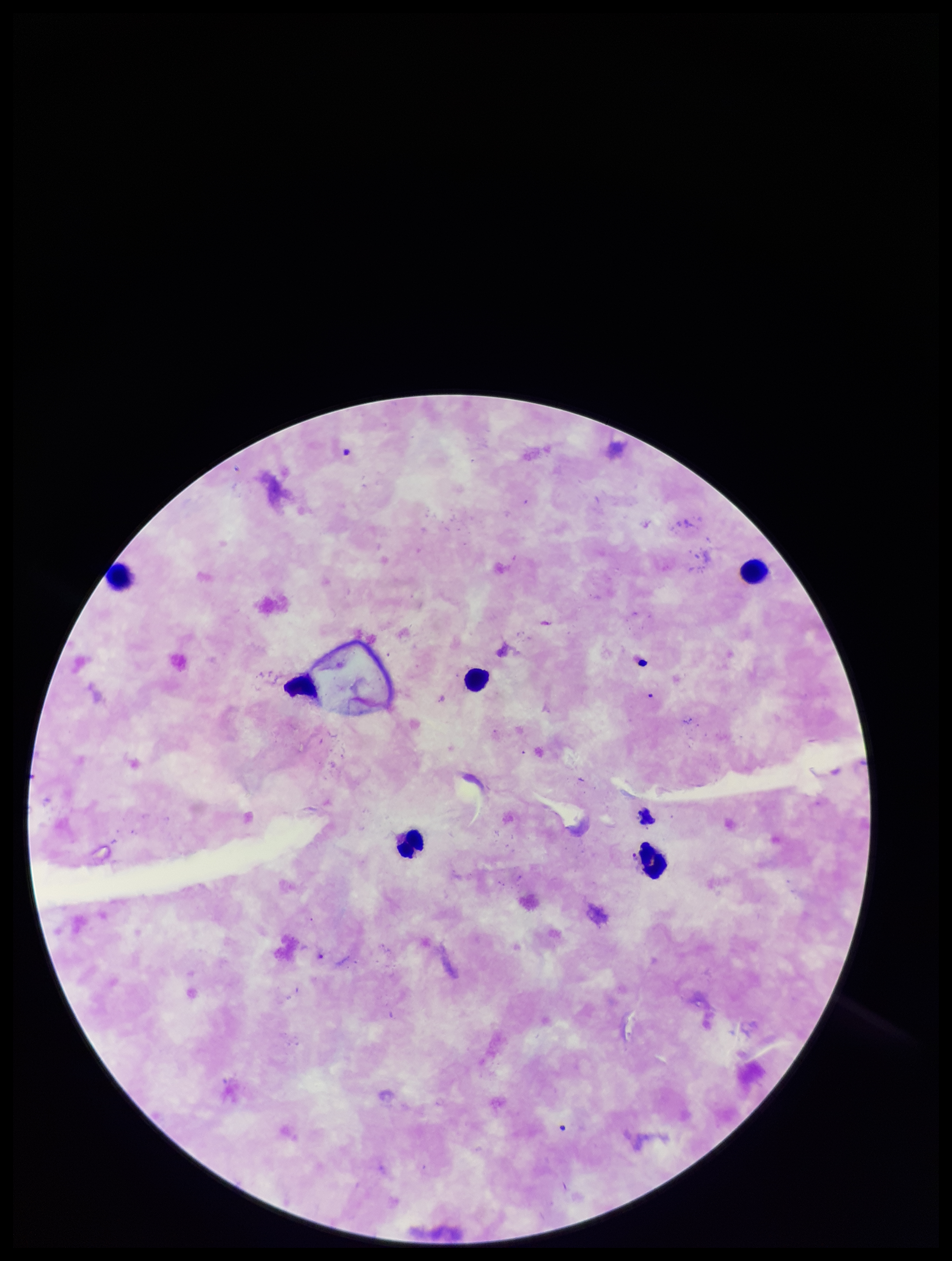 Image is 952×1261 pixels. Plasmodium parasites: none identified. Photographed through the microscope eyepiece with a smartphone camera. Giemsa stain. One field from this slide. Species reported for this patient: Plasmodium falciparum. Leukocyte count: 6. Preparation: thick. Parasite count: 0. Patient malaria status: positive.